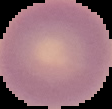

Summary:
  - Preparation: thin blood film
  - Image type: segmented cell region with the area outside set to black
  - Image size: 112×109 pixels
  - Malaria status: uninfected